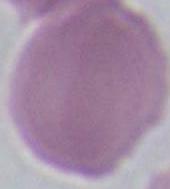
A red blood cell is seen. 1000x magnification. Micrograph.